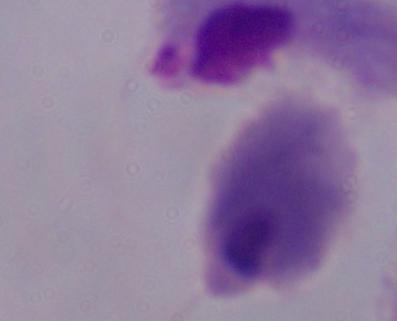

A trichomonad is seen. Captured at 1000x magnification. Photomicrograph.